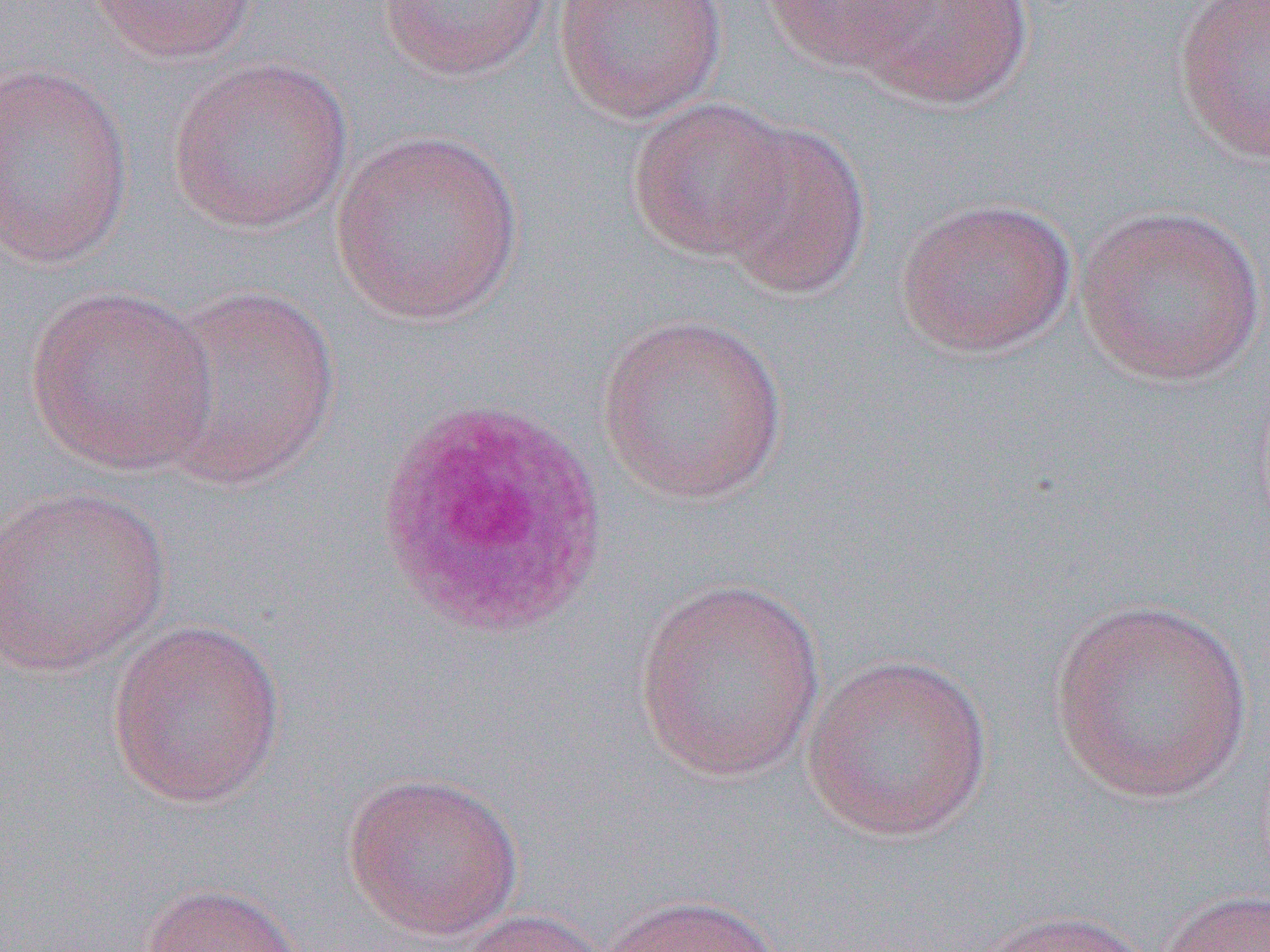
Approximate bounding boxes as [x1, y1, x2, y2] in pixels. Uninfected red blood cell locations: [86, 0, 263, 65], [551, 0, 729, 123], [759, 0, 936, 74], [847, 0, 1036, 110], [1172, 0, 1270, 166], [378, 1, 553, 81], [166, 57, 354, 235], [0, 62, 135, 271], [627, 97, 797, 263], [711, 120, 873, 301], [329, 129, 526, 327], [895, 196, 1079, 358], [1074, 204, 1266, 386], [25, 284, 218, 477], [148, 284, 342, 491], [596, 312, 789, 504], [0, 485, 173, 677], [633, 575, 828, 782], [1046, 597, 1256, 803], [106, 617, 286, 809], [800, 652, 993, 843], [342, 768, 524, 941], [138, 882, 310, 952], [1154, 888, 1270, 952], [595, 894, 785, 952], [450, 907, 612, 952], [966, 908, 1158, 952]. Slide-level diagnosis: Plasmodium vivax. One field of a larger specimen. Optical microscopy. Image is 1270×952 pixels. 1000x magnification. Thin blood smear.